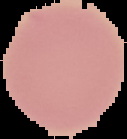

Summary:
  - Image type: cell region segmented out of the field of view; surrounding area masked to black
  - Preparation: thin blood film
  - Image size: 127×139 pixels
  - Result: no malaria parasites detected